Identify the preparation type.
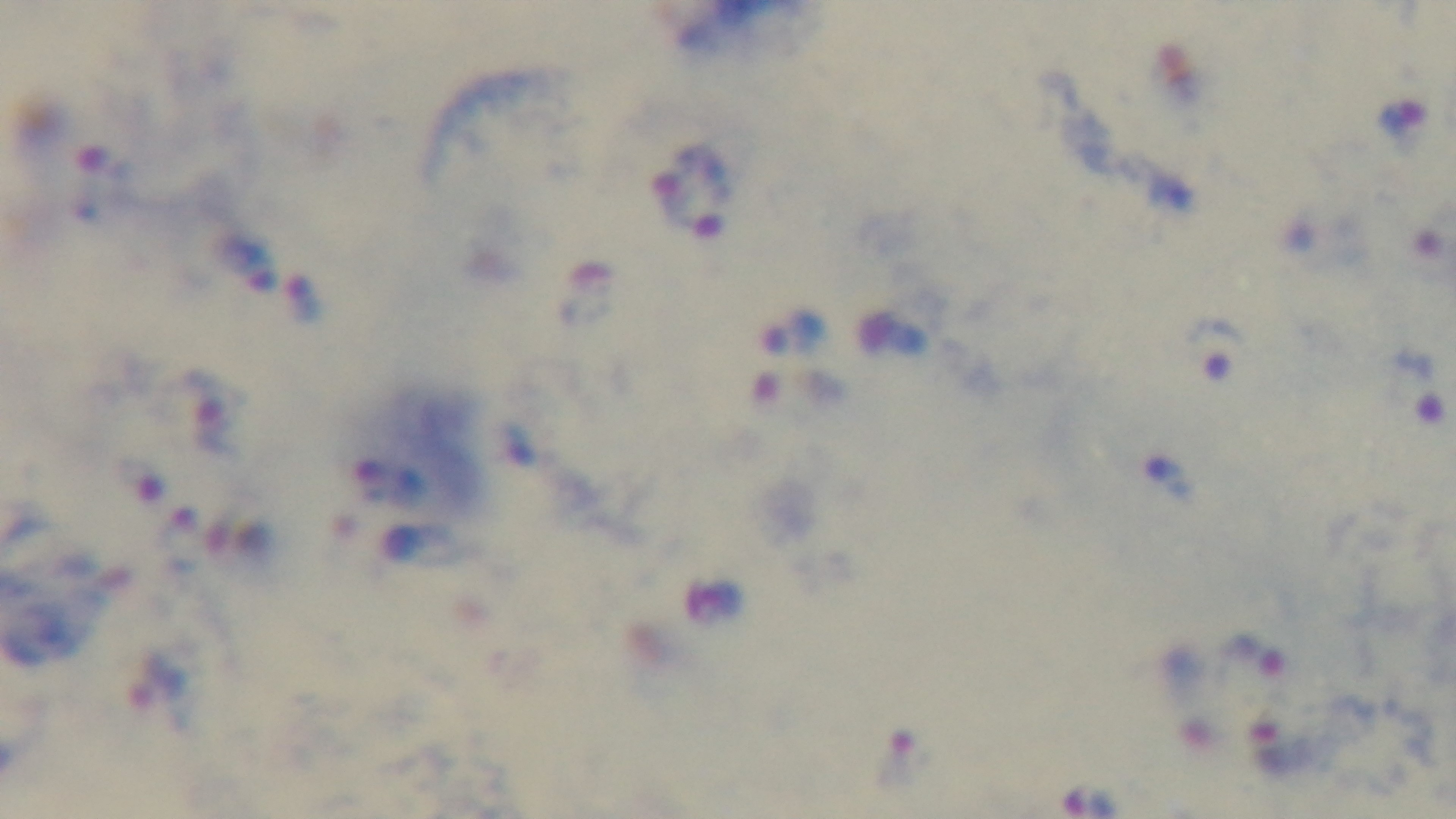
A thick smear.

Summary:
  - Objective: 100x oil immersion
  - Malaria status: positive
  - Stain: Giemsa
  - Field of view: single
  - Capture: mounted 4K digital camera
  - Modality: light microscopy